Look for Plasmodium parasites.
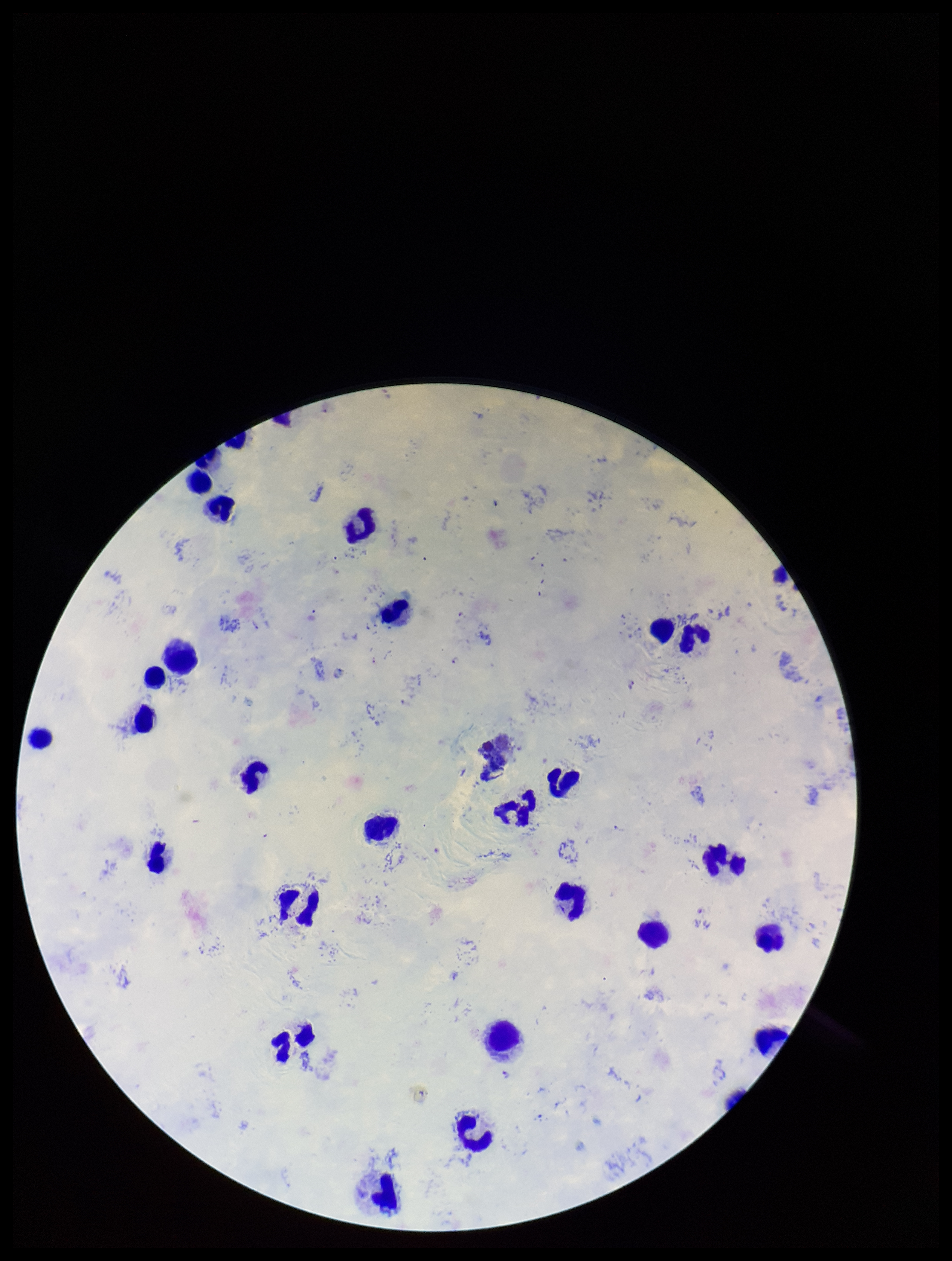
Seen.

Image is 952×1261 pixels. Species reported for this patient: Plasmodium falciparum. Leukocyte count: 27. Patient malaria status: infected. Parasite count: 4. Smartphone photograph taken through the eyepiece of a microscope. Stained with Giemsa. Preparation: thick. One field from this slide.